State which parasite is depicted.
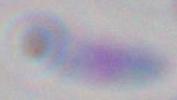
Toxoplasma gondii.

magnification = 1000x
modality = micrograph